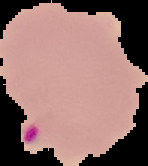
image type = cell region segmented out of the field of view; surrounding area masked to black
image size = 148×166 pixels
malaria status = parasitized
preparation = thin blood smear